Report the malaria status of this cell.
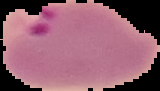
Parasitized.

{
  "image_type": "cell region segmented out of the field of view; surrounding area masked to black",
  "preparation": "thin blood smear",
  "image_size": "160×91 pixels"
}